Identify the preparation type.
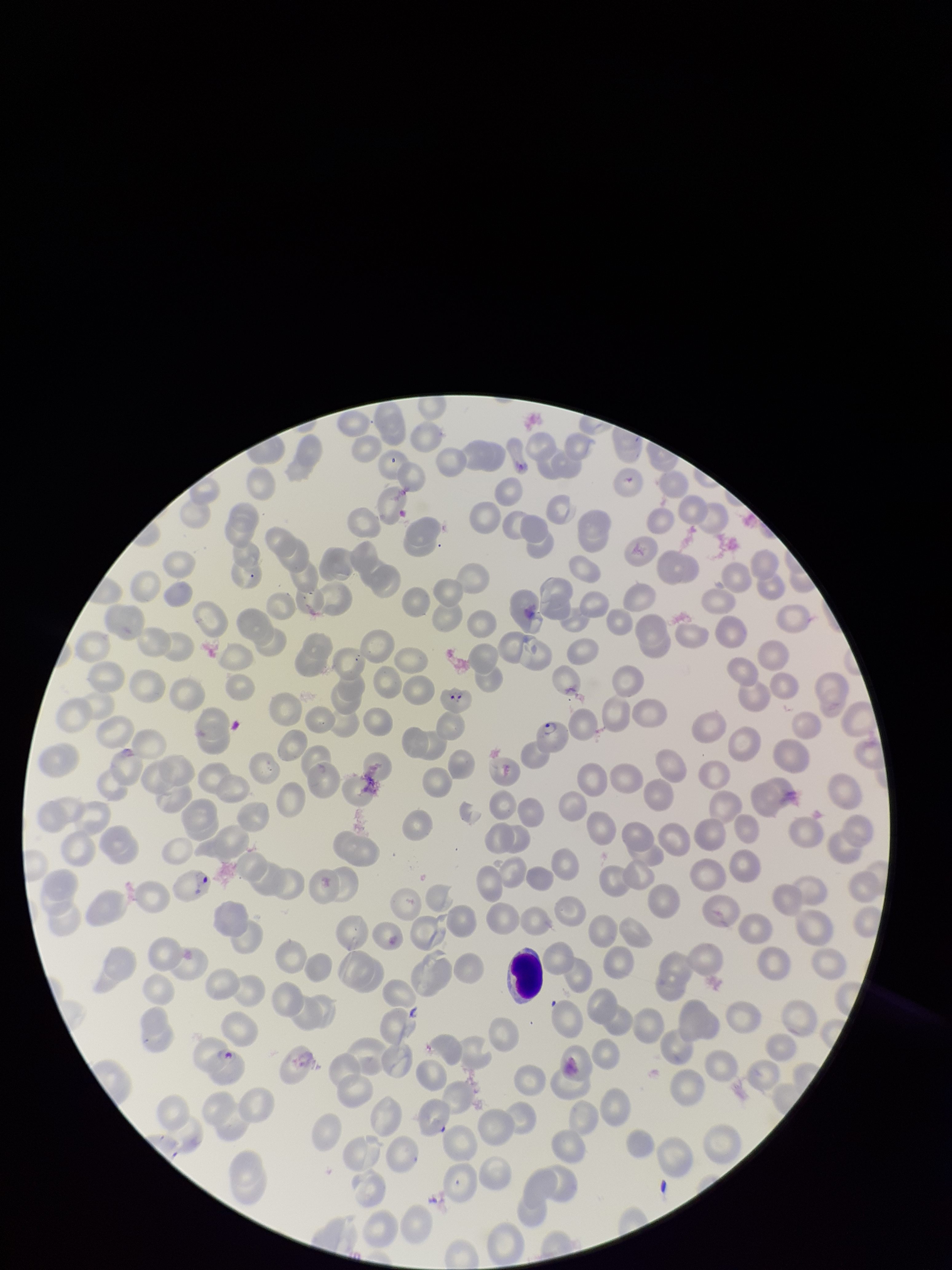

A thin smear.

Patient malaria status: positive. Parasitized red blood cells: detected. Stained with Giemsa. Single field of view. Species reported for this patient: Plasmodium falciparum. Smartphone photograph taken through the eyepiece of a microscope. Parasitized red blood cell count: 4. Image is 952×1270 pixels. Red blood cell count: 219.